Comment on the morphology of the erythrocytes.
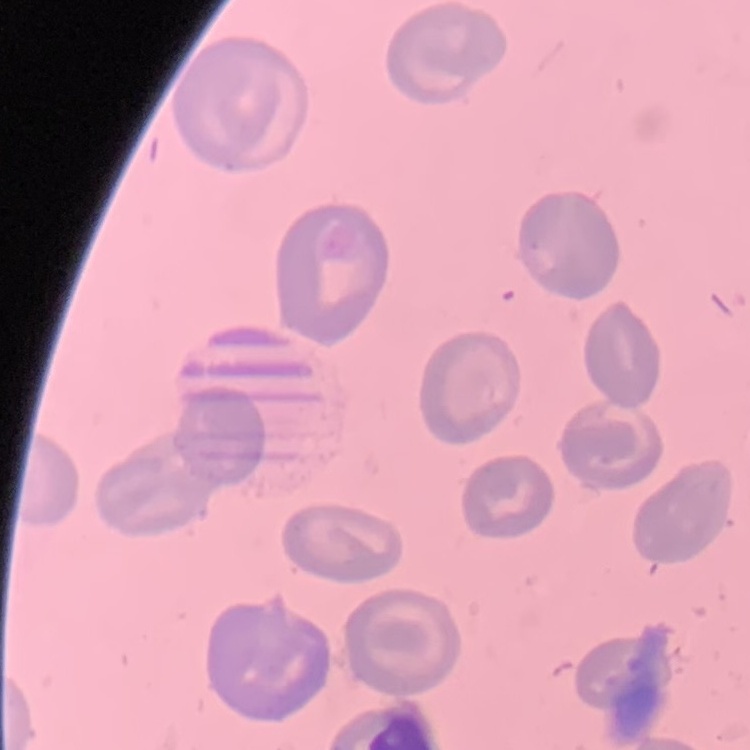
They show no rouleaux formation.

Summary:
  - Stain: Field's or Giemsa
  - Image type: one tile cut from a larger photomicrograph
  - Preparation: thin blood smear